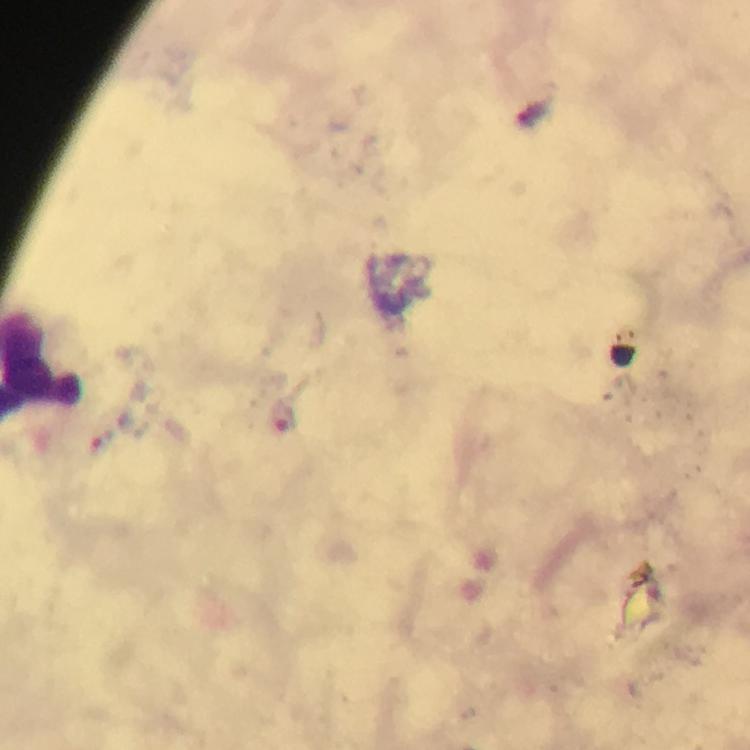
immersion oil = used
context = from a diagnostic examination for malaria
capture = smartphone photograph through a microscope
cropped from = one field of view
preparation = thick smear
image size = 750×750 pixels
magnification = 100x
malaria parasite locations = approximate centers as [x, y] in pixels: [283, 416], [106, 443]
stain = Giemsa